Locate and identify every blood parasite.
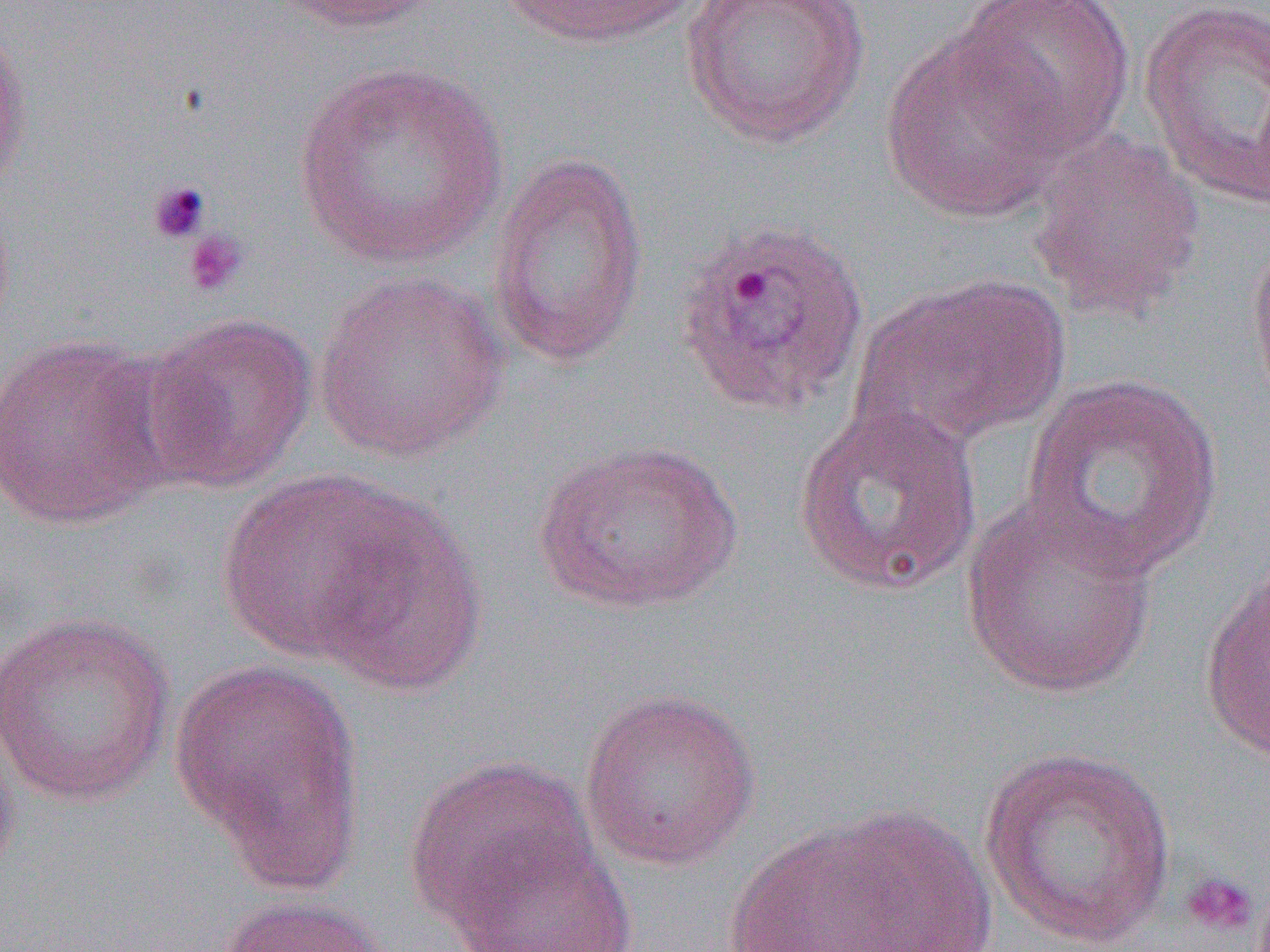
Approximate bounding boxes as (x1,y1)-(x2,y2) corner pairs in pixels.
Plasmodium ovale-infected red blood cells: (671,217)-(871,417).
No Plasmodium falciparum, Plasmodium malariae, Plasmodium vivax, Babesia divergens, or Trypanosoma brucei observed.

Summary:
  - Uninfected red blood cell locations: (274,0)-(447,33), (678,0)-(870,148), (951,0)-(1135,154), (1139,0)-(1269,211), (497,1)-(705,49), (0,17)-(33,202), (880,32)-(1076,225), (292,59)-(511,270), (1025,129)-(1206,323), (487,149)-(651,370), (1245,230)-(1270,412), (313,269)-(509,464), (855,273)-(1070,449), (141,312)-(317,492), (0,331)-(175,531), (1016,371)-(1227,581), (791,402)-(987,598), (531,439)-(745,615), (215,468)-(429,669), (961,497)-(1160,699), (307,498)-(489,697), (1199,558)-(1270,770), (0,610)-(176,806), (172,655)-(365,885), (579,686)-(762,872), (0,709)-(23,890), (978,746)-(1179,951), (402,754)-(604,937), (725,807)-(1005,952), (449,830)-(637,952), (214,894)-(392,952)
  - Platelet locations: (145,178)-(213,246), (181,228)-(249,299), (1178,869)-(1261,940)
  - Slide-level diagnosis: Plasmodium ovale
  - Magnification: 1000x
  - Modality: optical microscopy
  - Preparation: thin blood smear
  - Image size: 1270×952 pixels
  - Field of view: single